Report the malaria status.
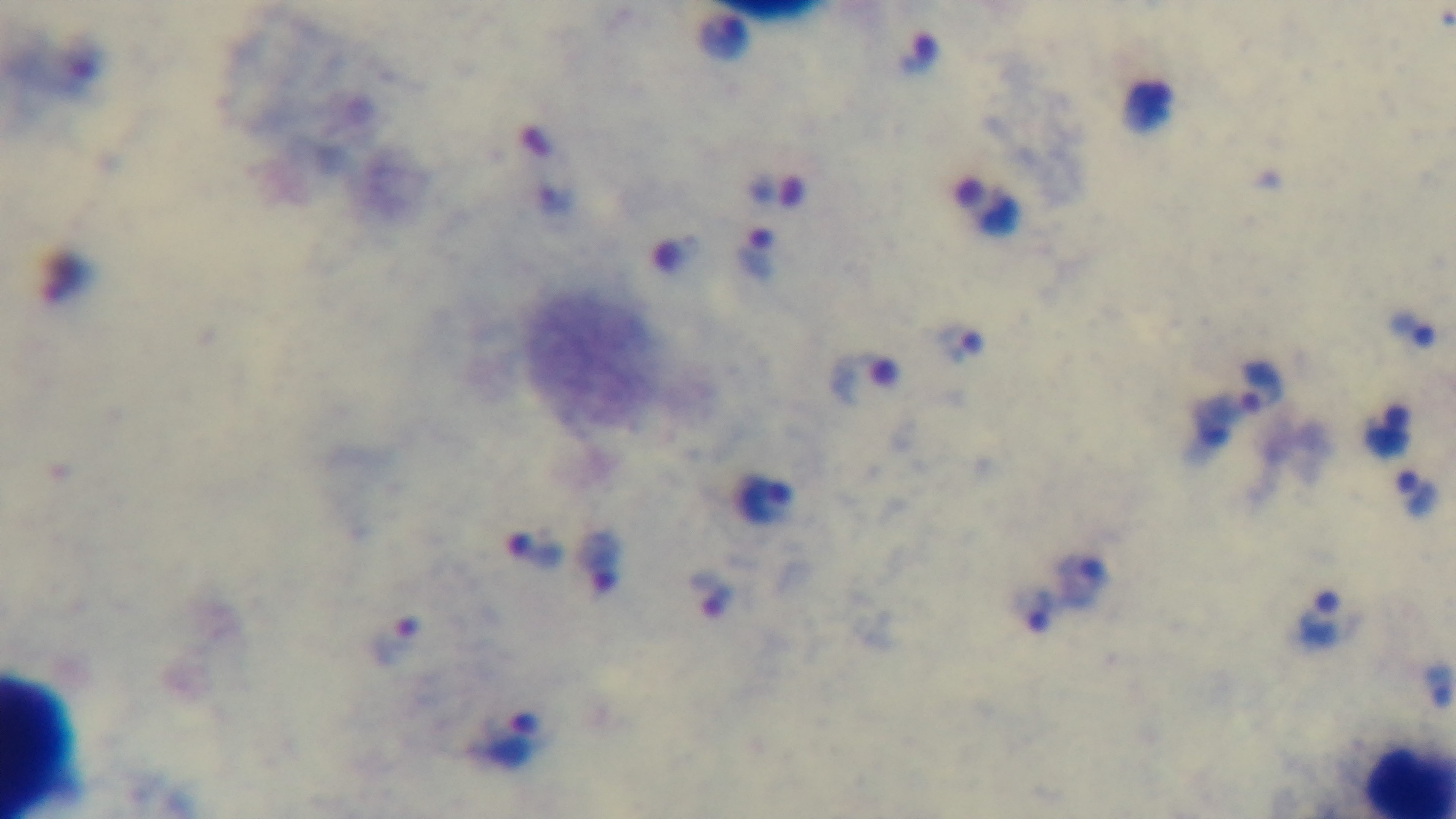
Positive.

modality = light microscopy
field of view = one from the slide
capture = mounted 4K digital camera
objective = 100x oil immersion
stain = Giemsa
preparation = thick blood film